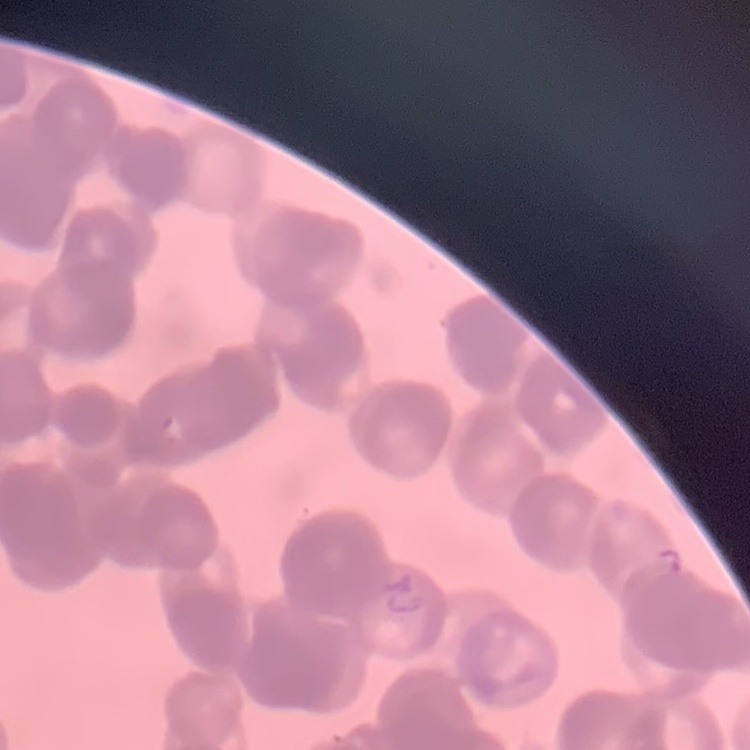

Summary:
  - Red blood cell morphology: rouleaux formation
  - Stain: Field's or Giemsa
  - Preparation: thin blood film
  - Image type: square crop of a larger photomicrograph